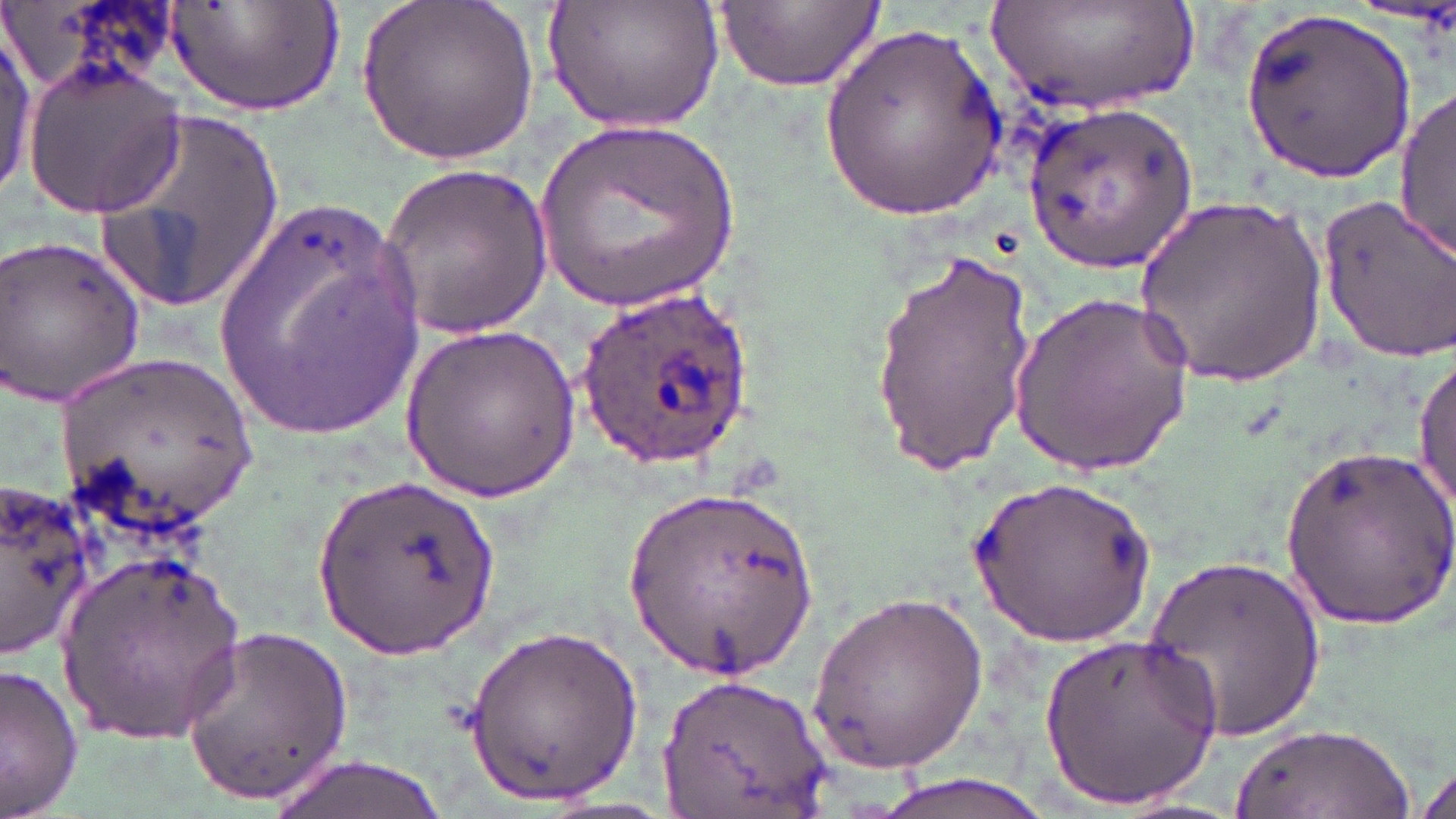 Approximate bounding boxes as [x1, y1, x2, y2] in pixels. Plasmodium ovale-infected red blood cell locations: [575, 283, 752, 468]. Uninfected red blood cell locations: [166, 0, 344, 119], [358, 0, 538, 164], [543, 0, 724, 133], [990, 1, 1203, 118], [716, 2, 883, 92], [1240, 9, 1418, 185], [1, 23, 36, 197], [819, 23, 1006, 218], [23, 61, 187, 219], [1394, 86, 1454, 262], [1023, 102, 1199, 269], [94, 103, 286, 313], [537, 118, 739, 314], [378, 164, 556, 337], [1316, 191, 1456, 364], [212, 192, 432, 440], [1134, 196, 1333, 382], [1, 229, 148, 408], [870, 245, 1035, 472], [1012, 289, 1193, 480], [400, 322, 580, 502], [54, 354, 258, 532], [1413, 355, 1455, 520], [1282, 442, 1456, 632], [311, 473, 499, 659], [0, 474, 102, 661], [967, 475, 1158, 650], [627, 489, 822, 670], [57, 548, 246, 746], [1143, 548, 1326, 746], [808, 587, 989, 777], [463, 620, 642, 809], [174, 624, 359, 803], [1039, 629, 1223, 812], [1, 660, 84, 819], [658, 675, 833, 814], [1231, 723, 1411, 817], [268, 752, 456, 819], [1411, 755, 1456, 819], [861, 773, 1069, 819]. Slide-level diagnosis: Plasmodium ovale. One field of a larger specimen. Image is 1456×819 pixels. Light microscopy. Thin blood film. May-Grünwald-Giemsa-stained preparation. Captured at 1000x magnification.